Report the malaria status of this cell.
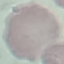

It is uninfected.

{
  "capture": "smartphone camera at the microscope eyepiece",
  "stain": "Giemsa",
  "image_type": "cell patch, automatically extracted from a larger field of view and resized to 64 × 64 pixels",
  "preparation": "thin blood smear"
}